Locate and identify every blood parasite.
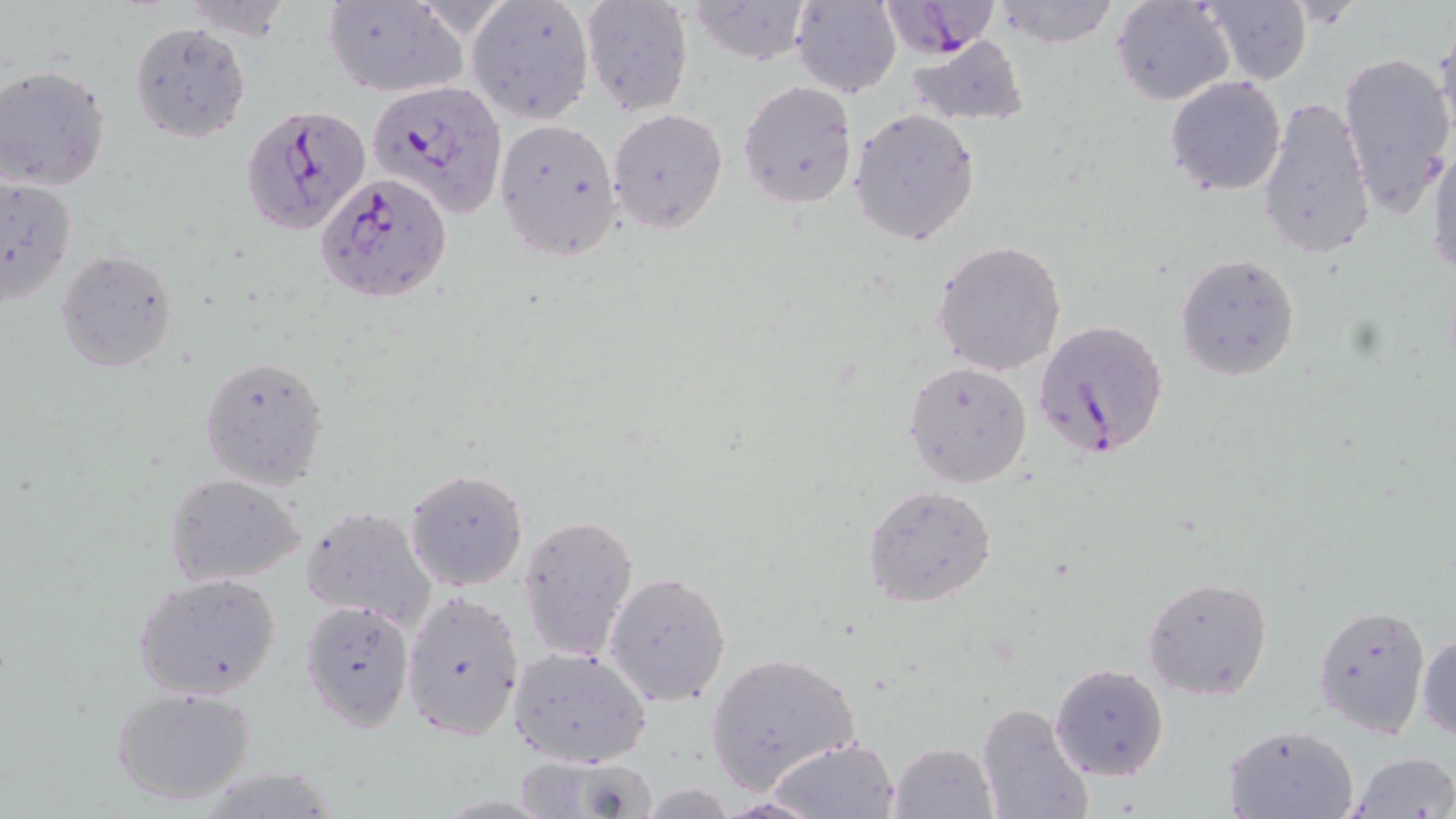

Approximate bounding boxes as named x1/y1/x2/y2 corners in pixels.
Plasmodium falciparum-infected red blood cells: (x1=878, y1=1, x2=1000, y2=57), (x1=367, y1=79, x2=509, y2=217), (x1=241, y1=104, x2=369, y2=236), (x1=318, y1=172, x2=453, y2=304), (x1=1034, y1=317, x2=1170, y2=461).
No Plasmodium ovale, Plasmodium malariae, Plasmodium vivax, Babesia divergens, or Trypanosoma brucei observed.

slide-level diagnosis = Plasmodium falciparum
stain = May-Grünwald-Giemsa
modality = light microscopy
preparation = thin blood film
field of view = one of a larger specimen
magnification = 1000x
uninfected red blood cell locations = approximate bounding boxes as named x1/y1/x2/y2 corners in pixels: (x1=990, y1=0, x2=1123, y2=48), (x1=1112, y1=0, x2=1236, y2=106), (x1=688, y1=1, x2=815, y2=65), (x1=792, y1=1, x2=901, y2=97), (x1=321, y1=2, x2=468, y2=98), (x1=579, y1=2, x2=694, y2=116), (x1=1196, y1=2, x2=1311, y2=85), (x1=467, y1=3, x2=593, y2=124), (x1=129, y1=21, x2=250, y2=143), (x1=1431, y1=26, x2=1456, y2=156), (x1=906, y1=35, x2=1031, y2=126), (x1=1338, y1=50, x2=1453, y2=213), (x1=1, y1=65, x2=115, y2=193), (x1=1164, y1=75, x2=1288, y2=196), (x1=737, y1=80, x2=858, y2=210), (x1=1257, y1=95, x2=1377, y2=260), (x1=607, y1=108, x2=728, y2=235), (x1=848, y1=109, x2=982, y2=247), (x1=493, y1=118, x2=623, y2=261), (x1=1426, y1=142, x2=1456, y2=278), (x1=0, y1=176, x2=75, y2=304), (x1=933, y1=240, x2=1067, y2=378), (x1=56, y1=249, x2=179, y2=373), (x1=1174, y1=253, x2=1301, y2=381), (x1=200, y1=355, x2=329, y2=489), (x1=903, y1=362, x2=1032, y2=487), (x1=404, y1=468, x2=529, y2=590), (x1=165, y1=472, x2=306, y2=589), (x1=863, y1=485, x2=997, y2=607), (x1=300, y1=505, x2=438, y2=632), (x1=517, y1=514, x2=639, y2=663), (x1=603, y1=571, x2=732, y2=706), (x1=131, y1=574, x2=282, y2=701), (x1=1142, y1=576, x2=1274, y2=700), (x1=401, y1=588, x2=525, y2=742), (x1=300, y1=599, x2=414, y2=730), (x1=1313, y1=603, x2=1432, y2=737), (x1=1416, y1=631, x2=1456, y2=743), (x1=509, y1=647, x2=650, y2=767), (x1=706, y1=651, x2=861, y2=793), (x1=1051, y1=664, x2=1169, y2=782), (x1=110, y1=685, x2=257, y2=806), (x1=976, y1=702, x2=1095, y2=819), (x1=1222, y1=724, x2=1359, y2=818), (x1=769, y1=736, x2=900, y2=818), (x1=889, y1=742, x2=997, y2=818), (x1=1349, y1=752, x2=1455, y2=819), (x1=511, y1=754, x2=659, y2=819)
image size = 1456×819 pixels